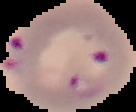

{
  "result": "malaria parasites detected",
  "preparation": "thin blood smear",
  "image_size": "136×112 pixels",
  "image_type": "segmented cell region with the area outside set to black"
}